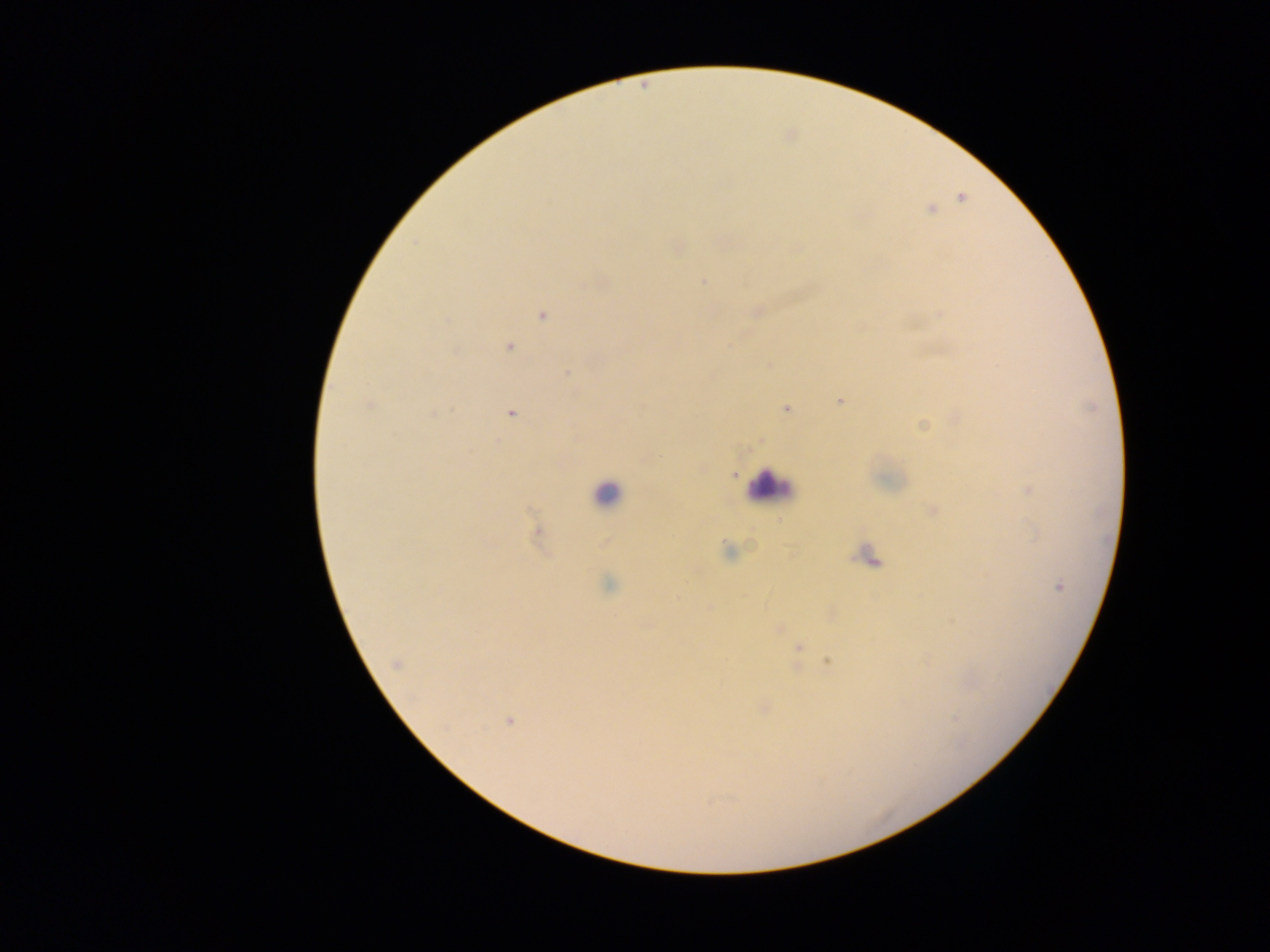
Approximate centers as x y in pixels. Leukocyte locations: 771 486; 607 494; 868 556. Plasmodium parasite locations: 961 197; 931 210; 678 248; 703 282; 757 311; 941 313; 542 314; 509 346; 768 363; 566 374; 838 401; 369 404; 787 408; 434 413; 511 413; 956 419; 922 425; 760 440; 702 468; 734 474; 1026 488; 933 510; 538 534; 606 543; 727 551; 609 585; 1058 586; 707 608; 831 614; 779 628; 798 648; 828 661; 396 663; 762 708; 508 721. Image is 1270×952 pixels. Thick blood film. One field of view. Sample from Ghana. Photographed through a microscope with a mobile-phone camera.